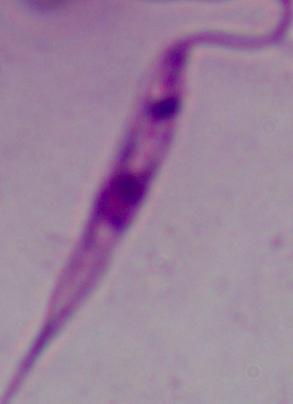 A Leishmania parasite is seen. Photomicrograph. Captured at 1000x magnification.